Identify the blood parasite species.
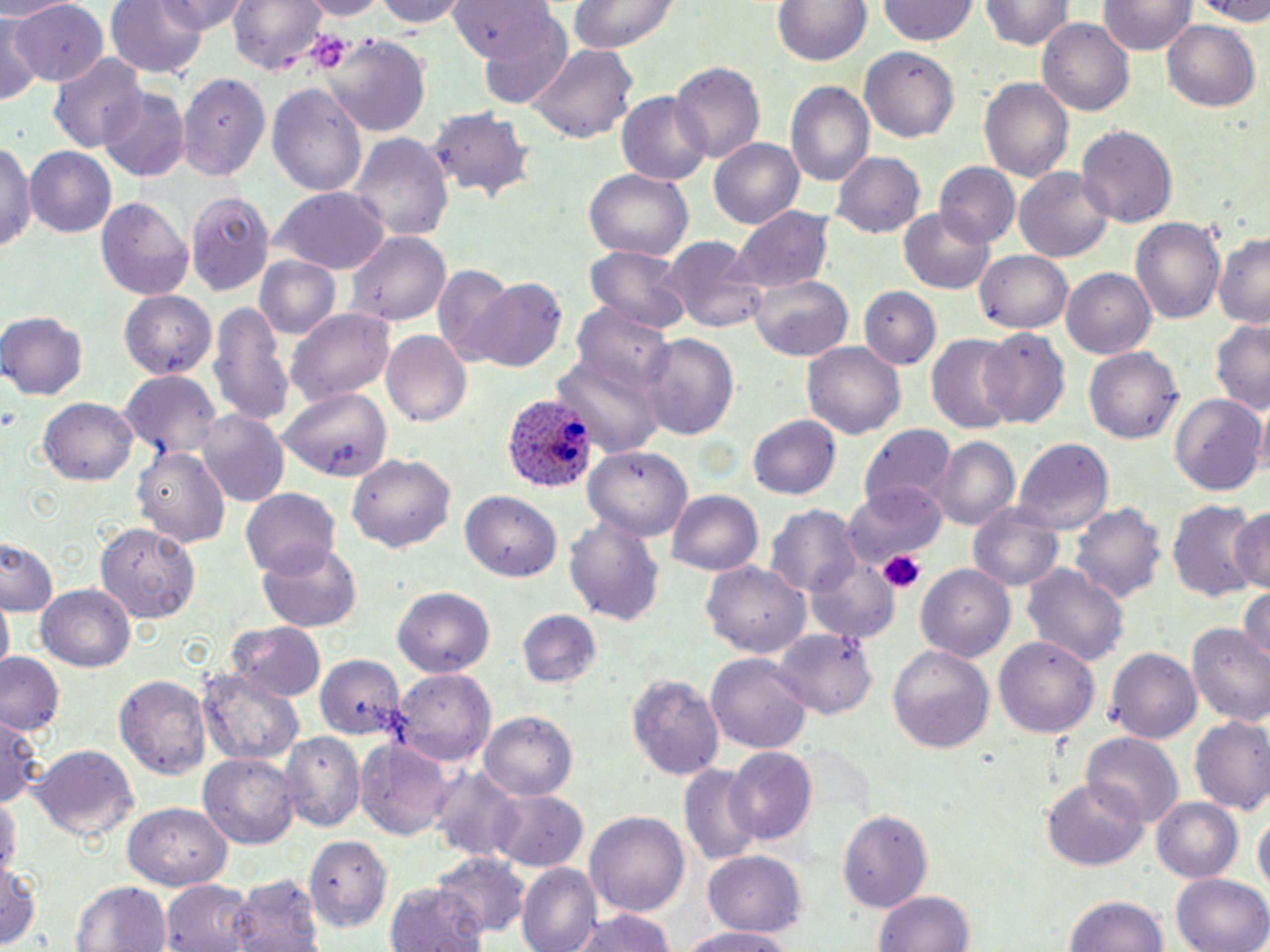
Plasmodium ovale.

image_size: 1270×952 pixels
plasmodium_ovale_infected_red_blood_cell_locations: 'approximate bounding boxes as (x1,y1)-(x2,y2) corner pairs in pixels: (503,394)-(597,493)'
modality: optical microscopy
preparation: thin blood film
platelet_locations: 'approximate bounding boxes as (x1,y1)-(x2,y2) corner pairs in pixels: (878,548)-(928,590)'
field_of_view: one of a larger specimen
magnification: 1000x
uninfected_red_blood_cell_locations: 'approximate bounding boxes as (x1,y1)-(x2,y2) corner pairs in pixels: (0,0)-(69,19), (105,0)-(209,77), (156,0)-(247,34), (229,0)-(324,76), (299,0)-(385,19), (367,0)-(471,26), (448,0)-(558,60), (568,0)-(678,56), (769,0)-(876,67), (878,0)-(978,46), (1187,0)-(1270,21), (980,1)-(1074,52), (1098,1)-(1195,54), (10,3)-(108,88), (125,4)-(243,57), (0,13)-(41,106), (477,16)-(574,109), (1038,18)-(1135,117), (1163,20)-(1261,112), (323,34)-(429,137), (526,43)-(637,144), (860,48)-(960,142), (46,50)-(145,154), (671,62)-(764,163), (176,71)-(274,182), (979,78)-(1073,181), (786,80)-(875,188), (268,82)-(368,195), (100,88)-(189,179), (617,91)-(714,186), (426,105)-(536,204), (1077,125)-(1177,227), (349,134)-(453,244), (709,137)-(804,229), (0,140)-(34,259), (0,145)-(87,250), (27,147)-(116,237), (833,152)-(926,240), (935,163)-(1020,246), (1015,165)-(1114,263), (584,169)-(692,262), (272,187)-(387,273), (188,193)-(272,295), (98,196)-(195,300), (900,205)-(996,294), (734,206)-(830,293), (1131,218)-(1226,324), (345,230)-(454,325), (1213,234)-(1270,327), (664,237)-(768,333), (584,245)-(694,333), (975,249)-(1073,334), (253,257)-(340,340), (432,265)-(514,363), (1061,268)-(1157,359), (747,271)-(853,361), (469,279)-(567,374), (861,288)-(940,369), (119,292)-(214,378), (210,299)-(292,424), (9,303)-(102,463), (575,303)-(677,400), (286,306)-(396,408), (1,313)-(88,400), (1209,318)-(1270,418), (977,327)-(1069,429), (381,330)-(470,427), (641,332)-(739,440), (926,333)-(1017,434), (803,342)-(906,440), (1085,344)-(1182,441), (555,349)-(665,457), (117,371)-(220,461), (279,390)-(393,481), (1170,394)-(1267,496), (40,397)-(137,485), (199,411)-(290,507), (748,415)-(842,501), (861,423)-(956,519), (933,435)-(1020,532), (1014,439)-(1113,533), (586,444)-(693,538), (134,445)-(230,546), (350,454)-(454,552), (846,484)-(943,569), (242,489)-(340,578), (668,489)-(765,576), (462,493)-(560,582), (1168,497)-(1262,605), (1073,501)-(1166,607), (968,503)-(1067,592), (1227,503)-(1269,599), (768,505)-(859,599), (565,515)-(664,626), (96,523)-(203,621), (1,535)-(61,613), (257,542)-(363,630), (805,553)-(902,646), (704,563)-(811,657), (916,563)-(1013,659), (1023,563)-(1128,672), (38,584)-(137,670), (391,585)-(494,677), (1240,585)-(1270,669), (0,598)-(12,672), (518,609)-(602,689), (228,622)-(326,701), (1188,626)-(1270,727), (772,627)-(878,721), (996,635)-(1101,737), (1105,646)-(1201,741), (888,648)-(995,754), (707,652)-(810,756), (0,655)-(62,736), (313,655)-(404,741), (201,665)-(305,768), (392,668)-(496,768), (628,671)-(726,784), (115,674)-(211,782), (0,710)-(44,813), (479,710)-(577,802), (1188,716)-(1270,816), (281,733)-(363,832), (1083,734)-(1182,827), (355,737)-(454,838), (28,745)-(139,841), (724,748)-(817,848), (200,753)-(299,849), (678,764)-(762,863), (429,767)-(522,860), (1042,778)-(1147,870), (488,787)-(588,871), (0,795)-(19,882), (1152,797)-(1243,882), (126,801)-(232,888), (586,809)-(689,919), (836,810)-(933,914), (1255,810)-(1268,902), (303,832)-(390,935), (705,851)-(805,936), (433,855)-(531,942), (0,859)-(43,947), (518,865)-(601,952), (1172,873)-(1270,952), (232,874)-(322,952), (161,879)-(258,952), (70,880)-(173,952), (384,880)-(487,952), (873,891)-(976,952), (1066,896)-(1169,952), (568,908)-(680,952), (678,925)-(799,952)'
stain: May-Grünwald-Giemsa